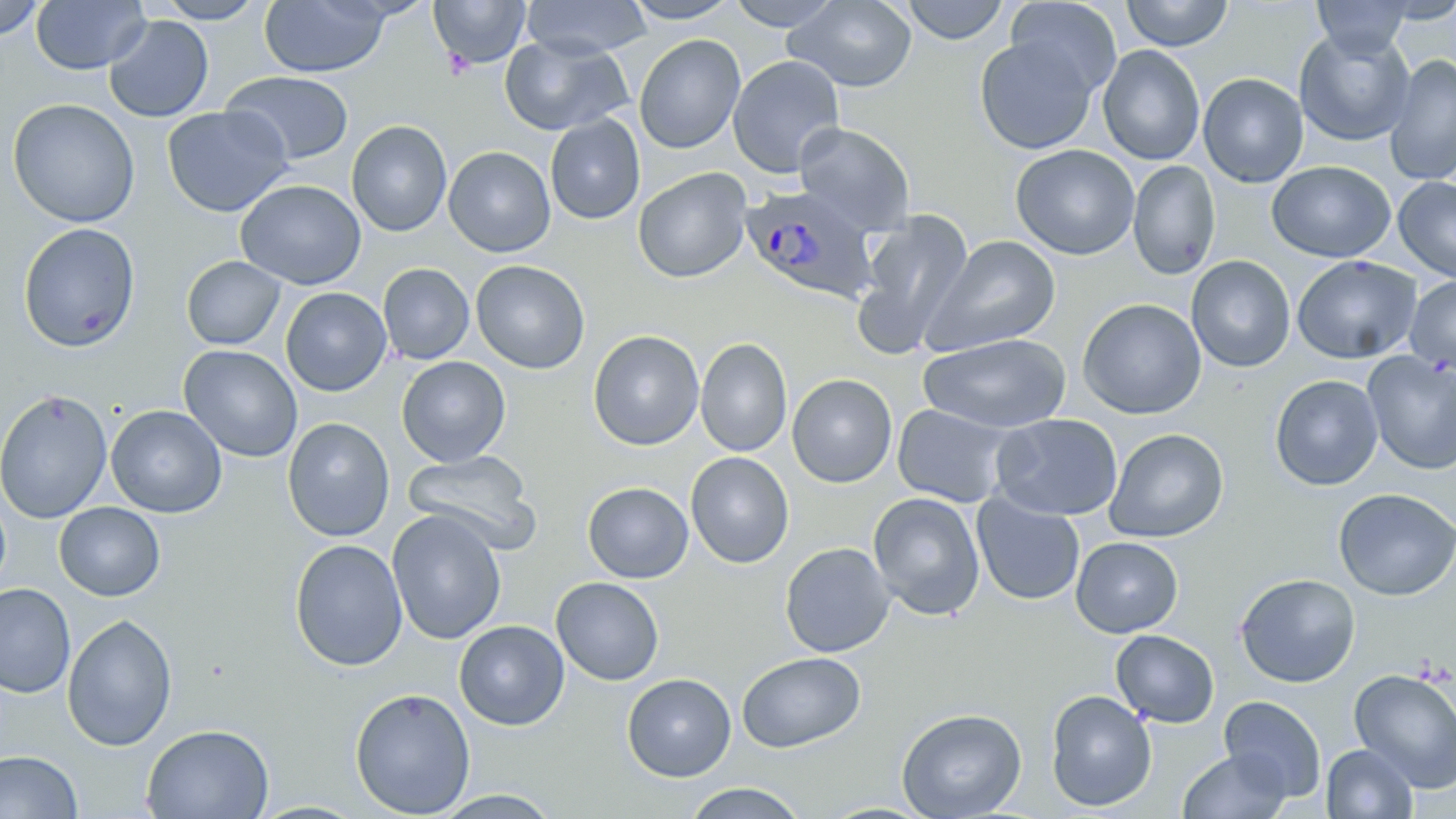

Summary:
  - Coordinate format: approximate bounding boxes as (x1, y1, x2, y2) in pixels
  - Plasmodium ovale-infected red blood cell locations: (738, 186, 882, 309)
  - Uninfected red blood cell locations: (31, 0, 149, 74), (152, 0, 267, 23), (429, 0, 530, 70), (521, 0, 651, 59), (622, 0, 741, 24), (726, 0, 843, 30), (784, 0, 918, 93), (901, 0, 1009, 45), (1005, 0, 1122, 99), (1120, 0, 1234, 51), (1311, 0, 1414, 58), (0, 1, 45, 41), (259, 1, 392, 78), (103, 15, 214, 123), (1294, 29, 1415, 146), (499, 34, 632, 136), (633, 34, 746, 154), (974, 35, 1098, 155), (1097, 45, 1205, 165), (728, 55, 845, 177), (1384, 56, 1456, 184), (220, 70, 356, 166), (1198, 72, 1308, 188), (7, 98, 140, 228), (162, 105, 292, 217), (544, 114, 646, 225), (346, 120, 452, 237), (793, 122, 915, 235), (1010, 144, 1140, 261), (443, 146, 556, 257), (1127, 160, 1221, 280), (1266, 161, 1395, 262), (633, 167, 753, 283), (1393, 177, 1456, 283), (235, 179, 367, 290), (856, 210, 974, 349), (18, 223, 140, 351), (923, 234, 1060, 354), (1186, 255, 1296, 373), (1291, 255, 1421, 364), (181, 256, 286, 350), (470, 260, 590, 374), (377, 263, 475, 365), (1405, 276, 1456, 374), (281, 287, 391, 397), (1076, 297, 1207, 419), (588, 330, 704, 451), (918, 335, 1072, 433), (695, 337, 792, 457), (179, 345, 303, 462), (1362, 352, 1456, 474), (396, 356, 511, 466), (787, 373, 897, 488), (1269, 374, 1383, 490), (0, 388, 113, 524), (891, 403, 1017, 508), (105, 404, 227, 518), (989, 413, 1123, 521), (282, 418, 395, 541), (1104, 428, 1229, 542), (402, 450, 542, 554), (685, 452, 794, 569), (581, 481, 694, 584), (1333, 488, 1456, 600), (0, 489, 11, 597), (867, 492, 986, 620), (971, 494, 1085, 606), (54, 502, 165, 601), (387, 510, 506, 644), (1070, 536, 1183, 638), (289, 538, 408, 671), (779, 542, 895, 658), (1235, 573, 1361, 687), (551, 576, 665, 686), (0, 583, 75, 698), (62, 613, 177, 751), (454, 620, 569, 731), (1110, 629, 1219, 728), (736, 652, 866, 752), (1348, 668, 1456, 793), (622, 673, 736, 781), (349, 687, 475, 818), (1045, 690, 1157, 811), (1219, 695, 1327, 802), (896, 707, 1027, 819), (141, 723, 274, 818), (1321, 744, 1417, 819), (1177, 748, 1292, 819), (0, 750, 82, 818), (681, 782, 809, 819), (430, 790, 563, 818)
  - Slide-level diagnosis: Plasmodium ovale
  - Magnification: 1000x
  - Field of view: single
  - Stain: May-Grünwald-Giemsa
  - Image size: 1456×819 pixels
  - Modality: optical microscopy
  - Preparation: thin blood film